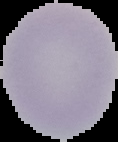
Summary:
  - Image type: cell region segmented out of the field of view; surrounding area masked to black
  - Image size: 118×142 pixels
  - Malaria status: uninfected
  - Preparation: thin blood film